Point out each Plasmodium parasite.
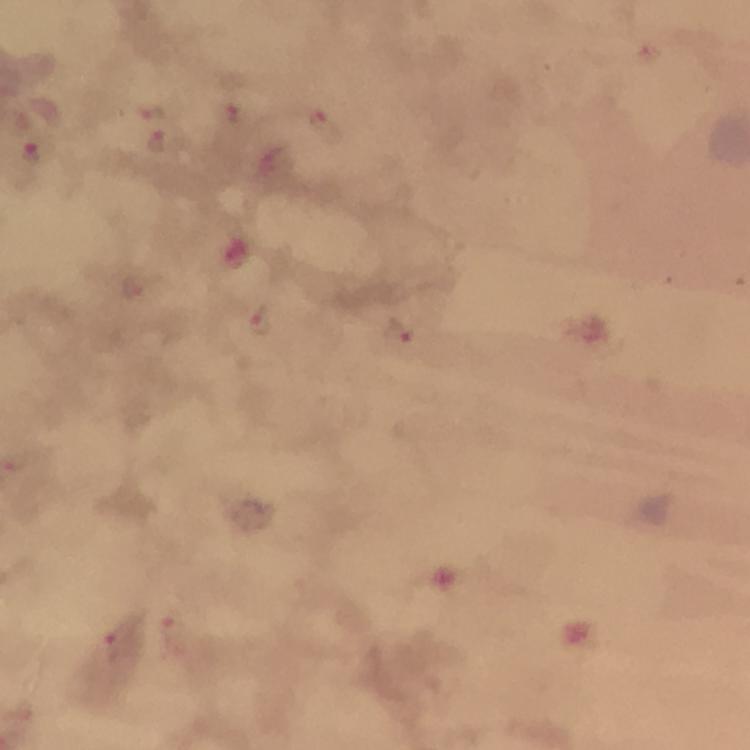
Approximate centers as {x, y} in pixels.
Plasmodium parasites: {646, 52}, {151, 111}, {239, 114}, {320, 122}, {157, 142}, {31, 158}, {258, 322}, {397, 335}, {174, 632}, {114, 645}.

100x magnification. From a diagnostic examination for malaria. Photographed through the microscope with a smartphone camera. Giemsa-stained preparation. Image is 750×750 pixels. Thick blood film. Immersion oil was used. A crop from one field of view.